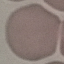

malaria status = uninfected
preparation = thin blood film
capture = smartphone through the microscope eyepiece
image type = automatically extracted cell patch, resized to 64 × 64 pixels
stain = Giemsa